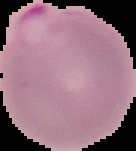
malaria status = parasitized
image size = 136×151 pixels
image type = segmented cell region with the area outside set to black
preparation = thin blood film